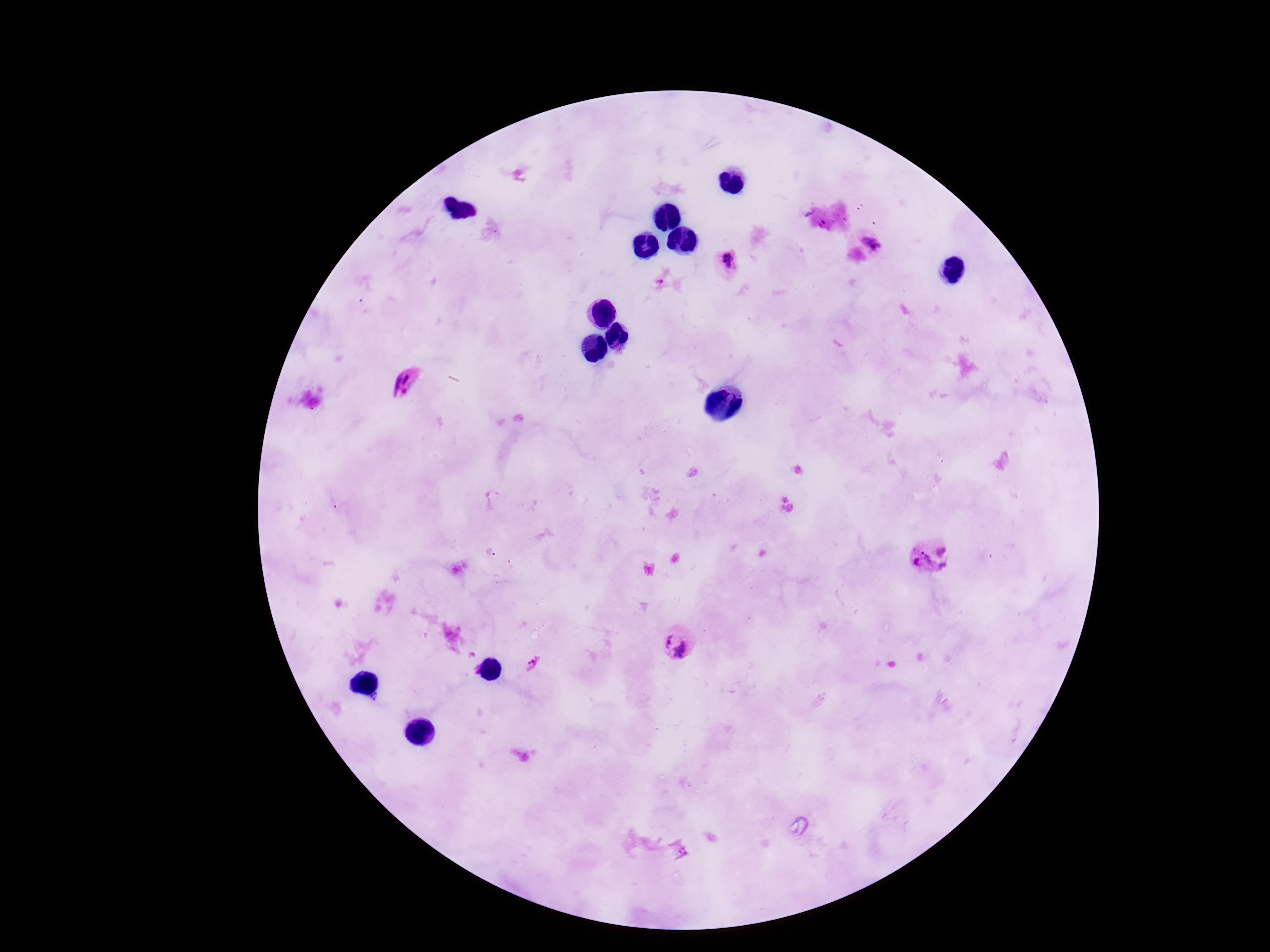 Approximate centers as {x, y} in pixels. Plasmodium parasite locations: {869, 237}, {728, 264}, {405, 382}, {930, 555}, {678, 643}. Photographed through the microscope eyepiece with a smartphone camera. Patient malaria status: infected. 100x magnification. Image is 1270×952 pixels. Giemsa-stained preparation. Single field of view. Thick peripheral-blood smear.